Outline each Trypanosoma brucei.
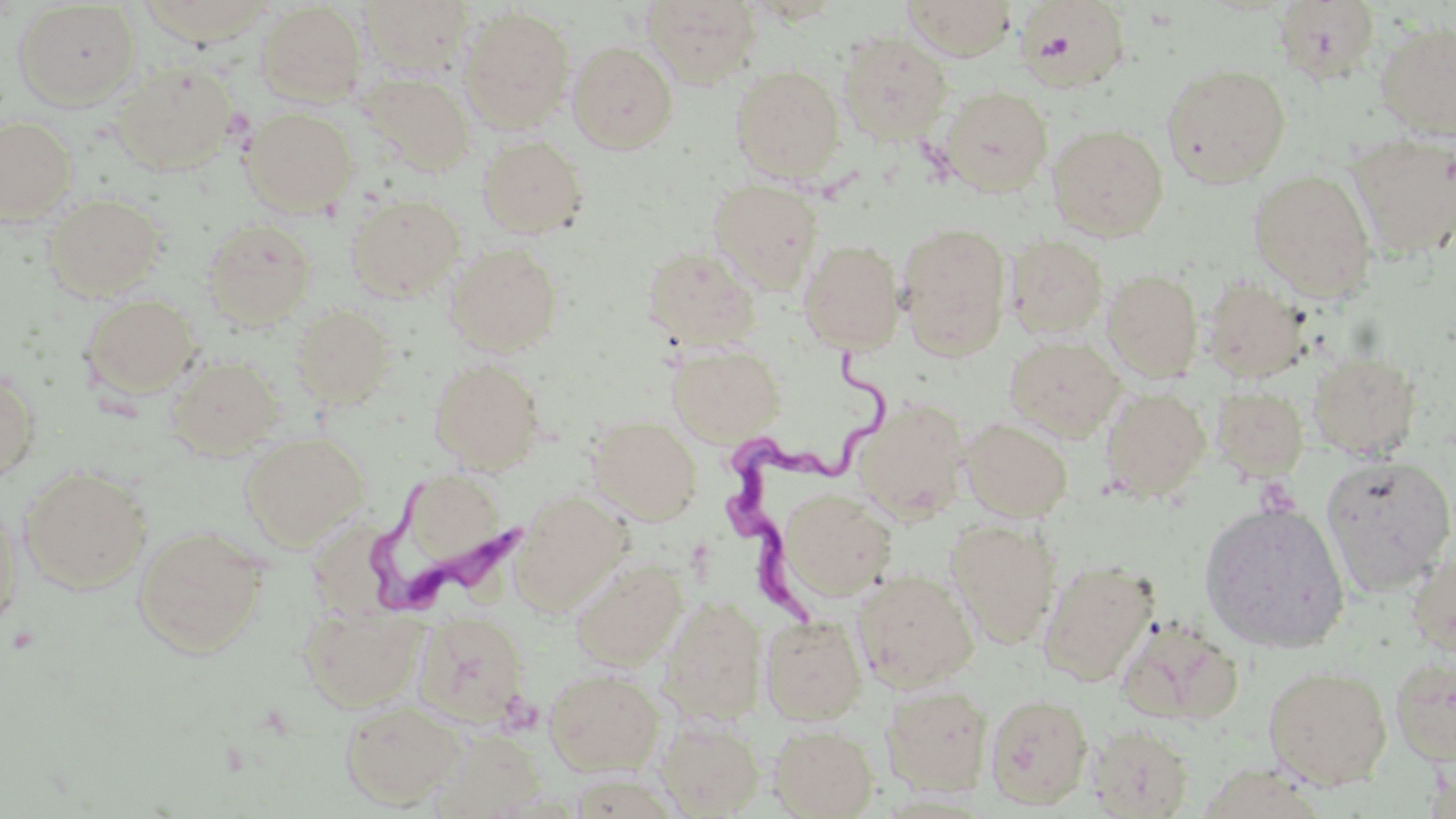

Approximate bounding boxes as (x1,y1)-(x2,y2) corner pairs in pixels.
Trypanosoma brucei: (717,348)-(897,632), (370,479)-(521,615).

Summary:
  - Uninfected red blood cell locations: (135,0)-(278,46), (359,0)-(475,77), (642,0)-(763,87), (902,0)-(1017,60), (1013,0)-(1133,93), (1273,1)-(1381,83), (13,2)-(141,109), (256,2)-(368,107), (458,6)-(576,133), (1375,20)-(1456,140), (836,30)-(953,145), (568,40)-(678,153), (111,61)-(239,175), (1161,63)-(1292,188), (731,65)-(845,183), (356,71)-(476,177), (939,86)-(1053,196), (241,107)-(358,216), (0,115)-(77,223), (1047,123)-(1169,241), (1348,131)-(1456,258), (477,134)-(588,238), (1248,168)-(1377,299), (708,179)-(824,291), (44,192)-(165,301), (345,193)-(466,303), (202,218)-(317,329), (897,222)-(1011,359), (1004,235)-(1109,340), (799,239)-(905,353), (444,242)-(563,356), (642,245)-(761,350), (1102,269)-(1203,382), (1203,277)-(1311,382), (81,294)-(200,399), (292,304)-(394,407), (1005,334)-(1124,441), (666,343)-(785,445), (1308,351)-(1422,461), (167,354)-(284,458), (429,358)-(545,472), (0,367)-(40,486), (1211,386)-(1309,480), (1100,387)-(1210,502), (854,400)-(969,522), (588,416)-(702,524), (960,417)-(1073,521), (239,431)-(369,550), (1323,454)-(1455,595), (19,467)-(152,594), (395,470)-(511,574), (780,488)-(896,601), (511,490)-(632,615), (1199,501)-(1350,654), (0,502)-(22,634), (946,518)-(1060,649), (132,525)-(269,658), (1406,547)-(1456,660), (572,557)-(687,670), (1039,559)-(1159,686), (852,567)-(980,691), (659,595)-(766,725), (299,604)-(426,711), (414,610)-(530,728), (761,615)-(867,724), (1115,616)-(1244,727), (1390,652)-(1456,766), (1263,664)-(1392,790), (544,667)-(664,777), (882,685)-(993,797), (985,692)-(1094,809), (340,699)-(465,809), (656,717)-(763,817), (769,723)-(878,818), (1087,723)-(1195,818), (435,730)-(546,818)
  - Slide-level diagnosis: Trypanosoma brucei
  - Modality: optical microscopy
  - Image size: 1456×819 pixels
  - Magnification: 1000x
  - Field of view: single
  - Preparation: thin blood smear
  - Stain: May-Grünwald-Giemsa